Evaluate for Plasmodium parasites.
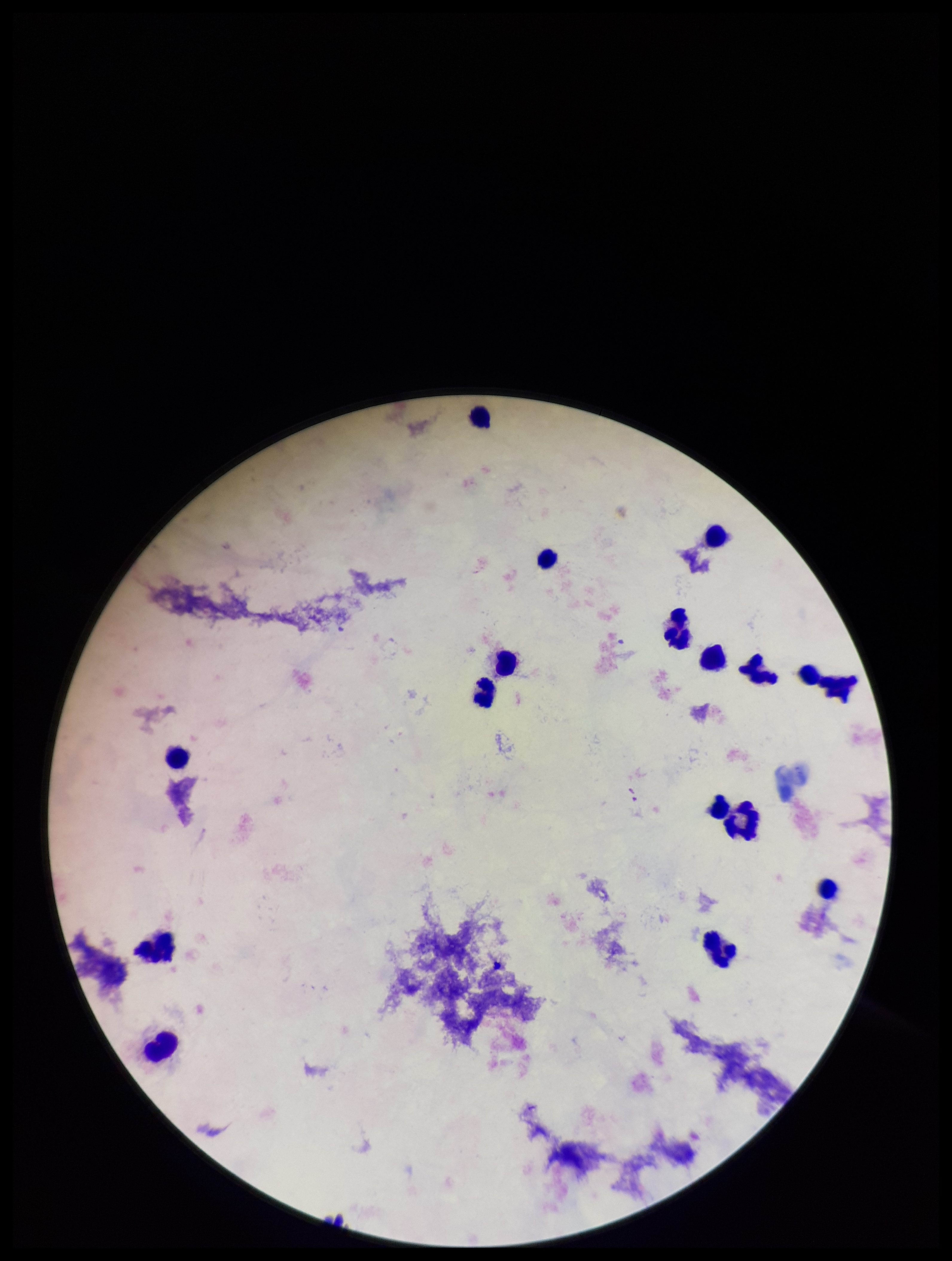

None detected.

{
  "field_of_view": "single",
  "preparation": "thick",
  "parasite_count": 0,
  "image_size": "952×1261 pixels",
  "leukocyte_count": 18,
  "patient_malaria_status": "negative",
  "stain": "Giemsa",
  "capture": "smartphone photograph through the microscope eyepiece"
}